Look for Plasmodium parasites.
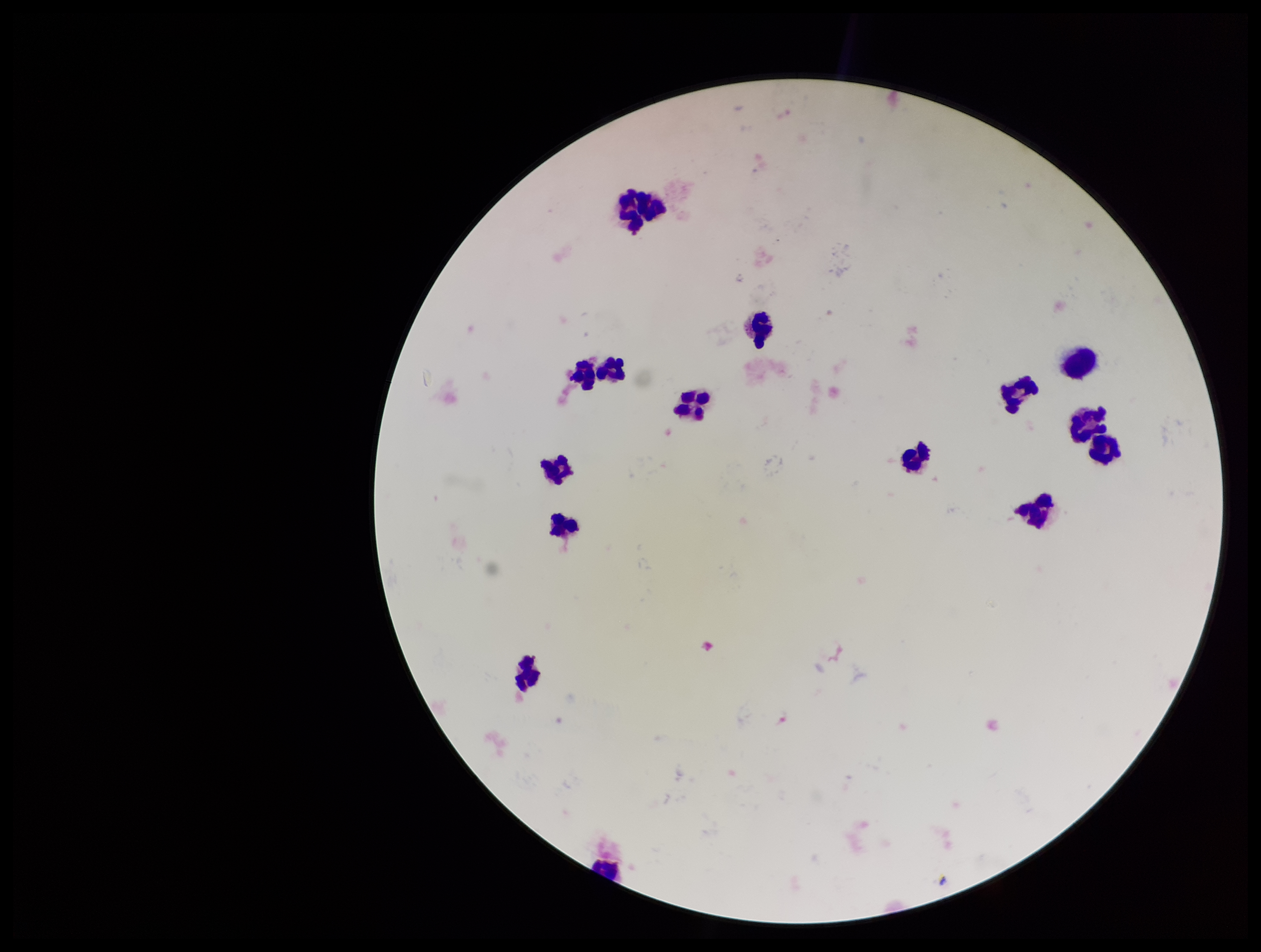

None identified.

capture = smartphone photograph through the microscope eyepiece
stain = Giemsa
image size = 1261×952 pixels
patient malaria status = negative
leukocyte count = 14
preparation = thick
field of view = one from this slide
parasite count = 0